Report the malaria status.
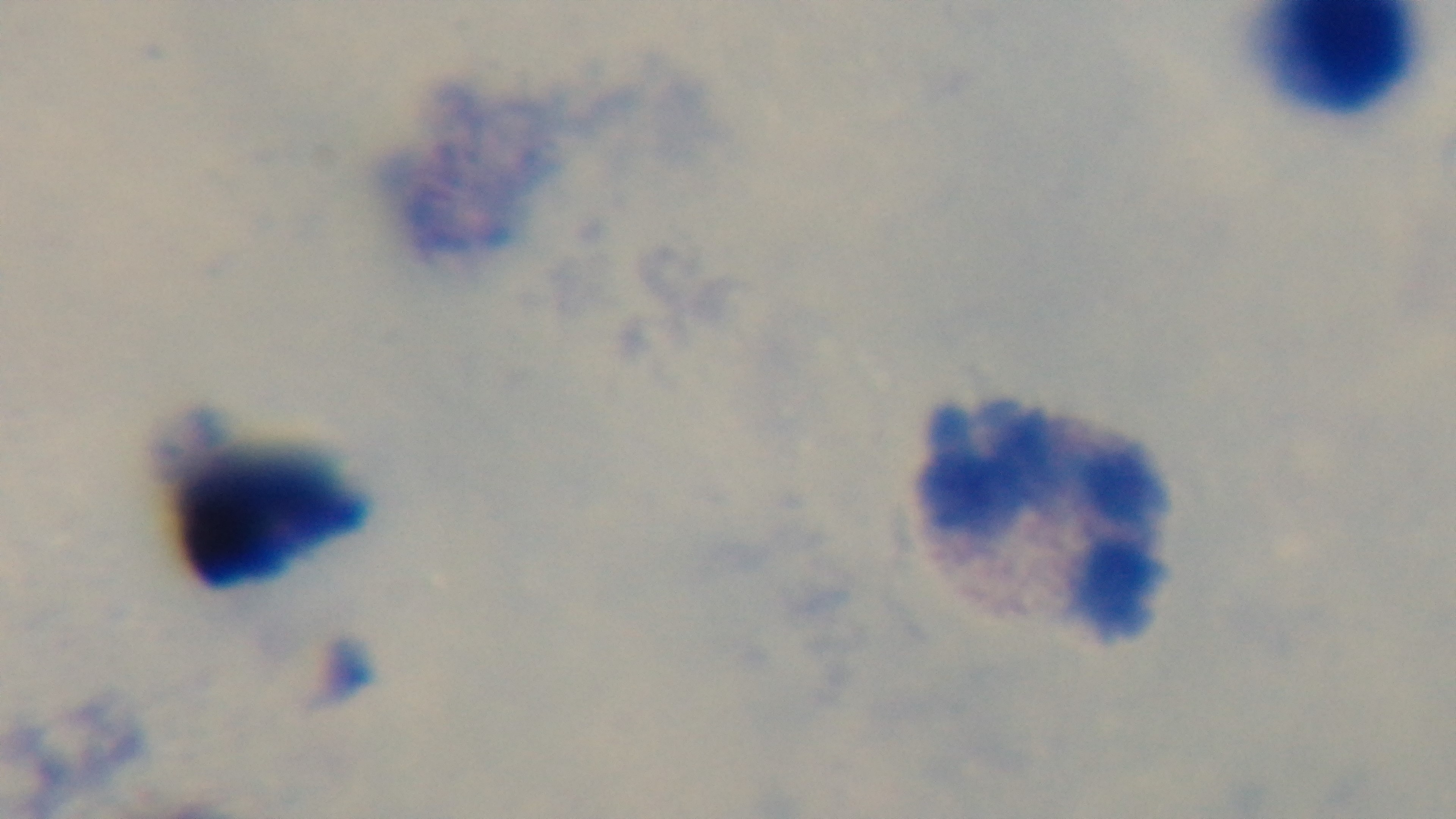
Uninfected.

modality = light microscopy
field of view = single
objective = 100x oil immersion
capture = mounted 4K digital camera
stain = Giemsa
preparation = thick